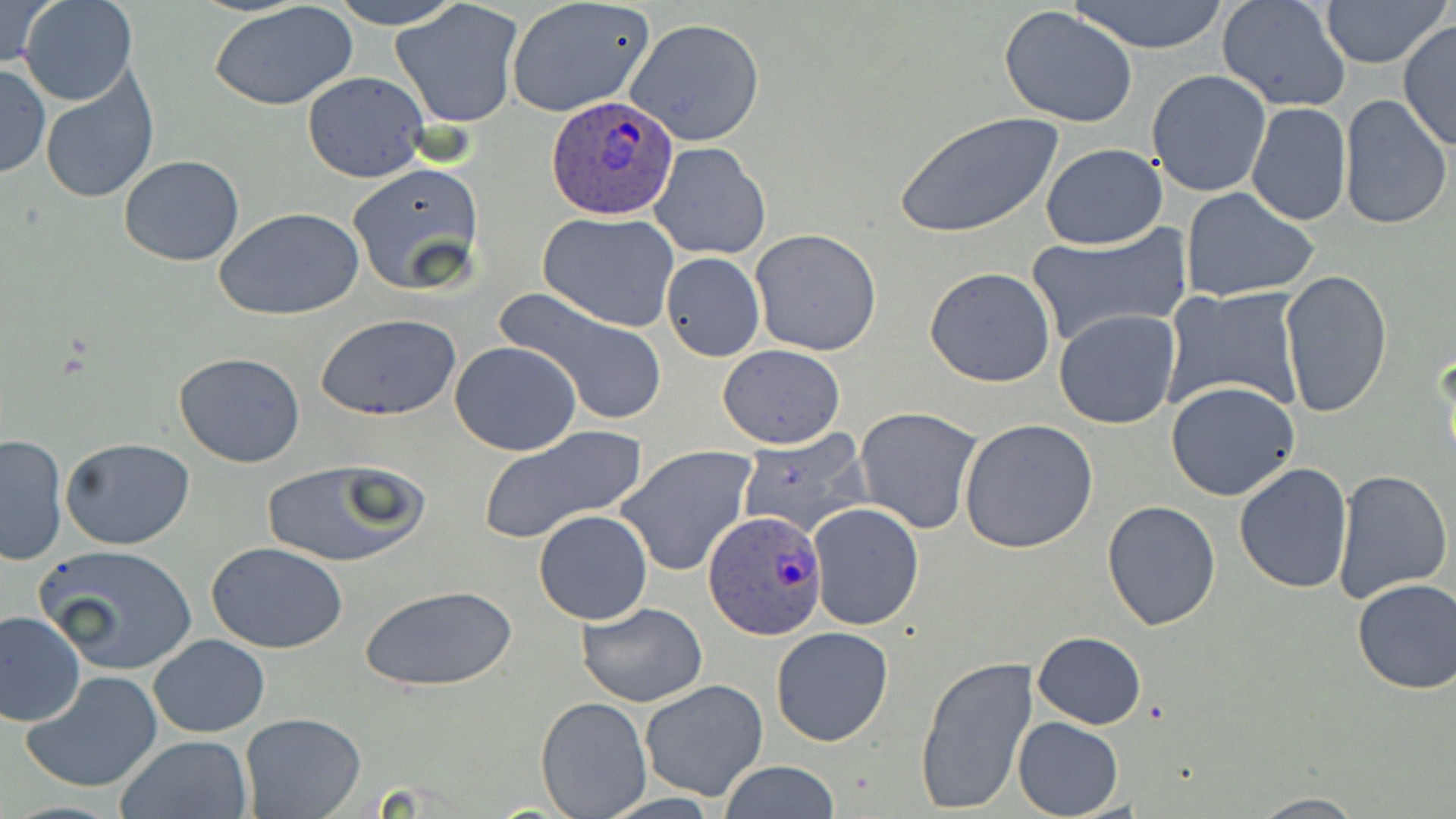

Summary:
  - Coordinate format: approximate bounding boxes as (x1,y1)-(x2,y2) corner pairs in pixels
  - Plasmodium ovale-infected red blood cell locations: (547,95)-(679,220), (703,510)-(829,641)
  - Uninfected red blood cell locations: (0,0)-(52,71), (19,0)-(138,105), (325,0)-(466,28), (505,0)-(656,119), (1065,0)-(1234,54), (1216,0)-(1352,113), (1318,0)-(1451,68), (211,1)-(359,111), (394,4)-(522,126), (999,6)-(1138,128), (626,18)-(766,145), (1397,18)-(1456,151), (0,60)-(50,179), (40,66)-(160,206), (1147,70)-(1271,195), (302,71)-(430,184), (1337,94)-(1453,232), (1247,102)-(1350,225), (895,112)-(1067,238), (651,142)-(770,260), (1039,142)-(1167,249), (118,155)-(245,267), (347,162)-(487,295), (1180,188)-(1320,302), (214,206)-(364,321), (538,212)-(679,331), (1025,227)-(1190,348), (749,229)-(882,357), (661,253)-(764,361), (924,266)-(1057,387), (1279,270)-(1393,416), (496,285)-(671,428), (1160,287)-(1304,418), (1053,309)-(1180,429), (316,314)-(461,421), (450,341)-(581,456), (718,345)-(845,450), (173,352)-(307,467), (1166,382)-(1299,502), (855,407)-(981,534), (959,420)-(1100,555), (478,425)-(649,544), (737,429)-(875,541), (0,433)-(68,566), (62,437)-(195,550), (612,445)-(758,578), (259,460)-(427,566), (1233,461)-(1355,594), (1331,468)-(1455,604), (1101,499)-(1220,632), (808,503)-(924,631), (532,510)-(653,625), (207,541)-(349,652), (35,542)-(197,674), (1351,577)-(1456,693), (360,584)-(518,691), (575,600)-(707,706), (1,610)-(86,726), (770,627)-(895,747), (1031,630)-(1146,728), (149,635)-(270,737), (916,654)-(1037,816), (21,671)-(165,795), (639,679)-(768,802), (535,697)-(650,817), (239,710)-(365,818), (1013,717)-(1124,818), (115,734)-(254,819), (718,760)-(839,819), (1246,793)-(1368,817)
  - Slide-level diagnosis: Plasmodium ovale
  - Modality: light microscopy
  - Stain: May-Grünwald-Giemsa
  - Image size: 1456×819 pixels
  - Magnification: 1000x
  - Field of view: single
  - Preparation: thin blood film